Assess this cell for malaria.
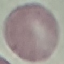
It is uninfected.

Cell patch, automatically extracted from a larger field of view and resized to 64 × 64 pixels. Photographed with a smartphone camera at the microscope eyepiece. Thin blood smear. Giemsa stain.